Assess this cell for malaria.
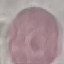

Uninfected.

stain = Giemsa
preparation = thin smear
image type = cell patch, automatically extracted from a larger field of view and resized to 64 × 64 pixels
capture = smartphone through the microscope eyepiece